Assess the morphology of the erythrocytes.
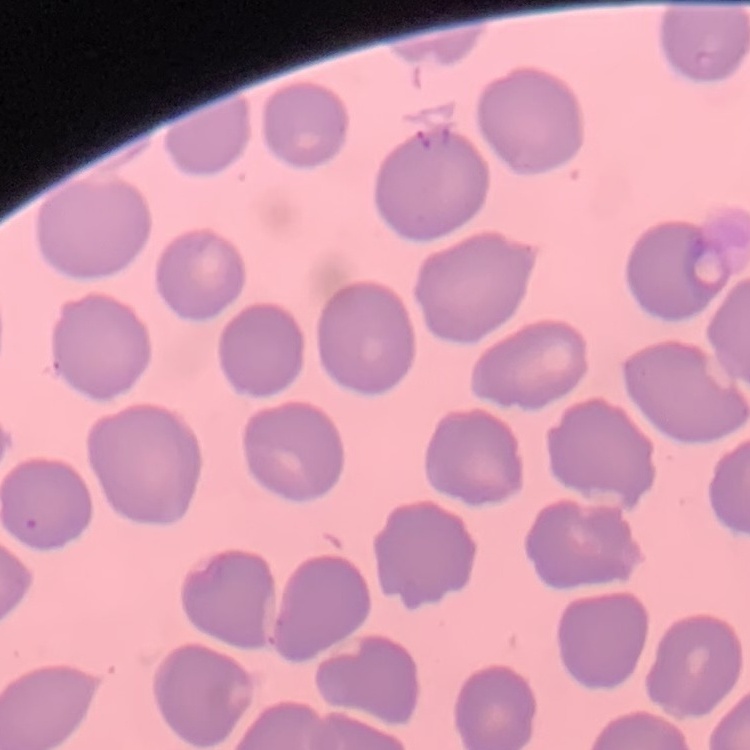
They show no rouleaux formation.

image_type: square crop of a larger photomicrograph
stain: Field's or Giemsa
preparation: thin blood smear